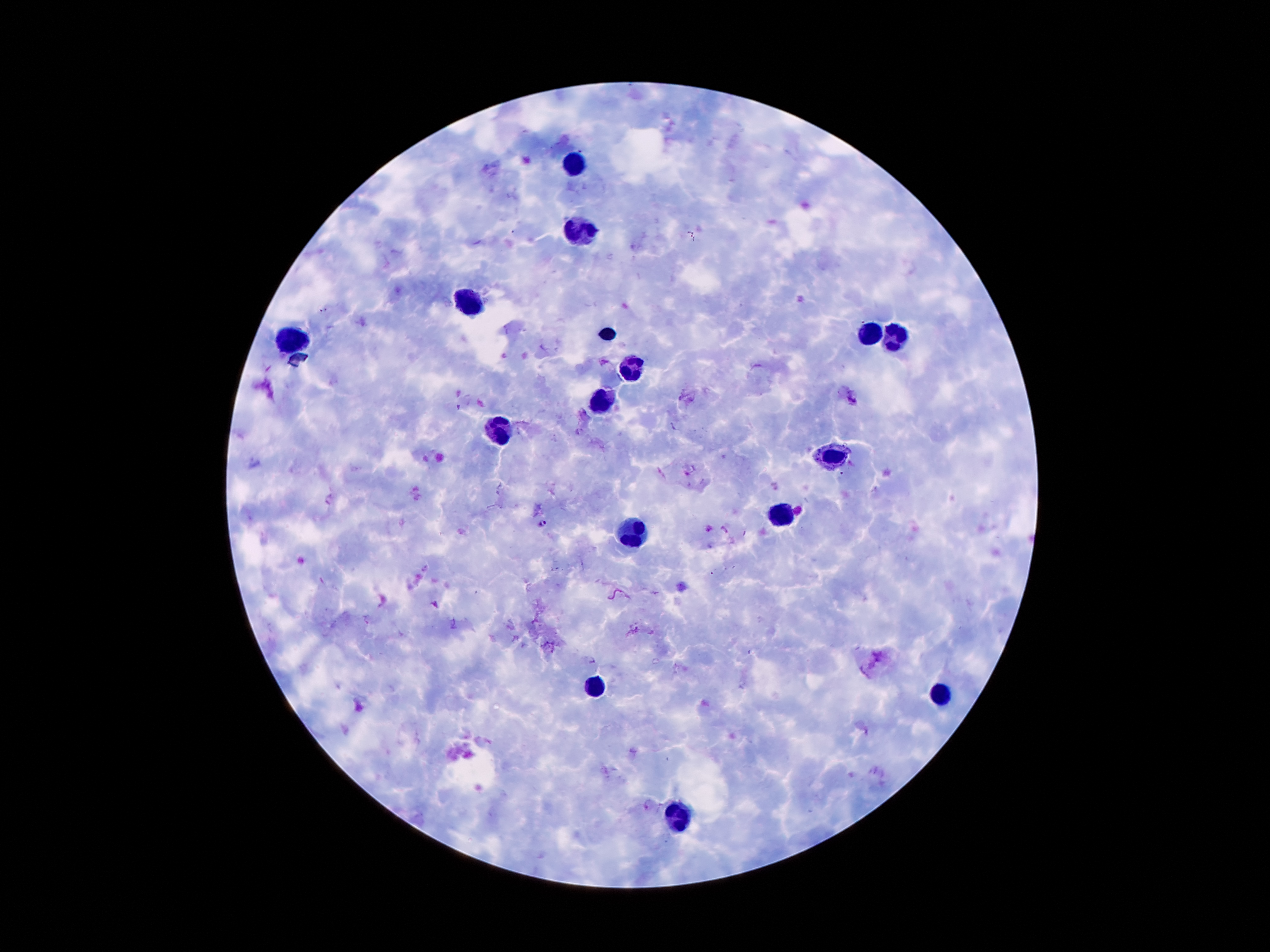

Approximate centers as (x, y) in pixels. Malaria parasite locations: (542, 523). Leukocyte locations: (574, 159), (579, 229), (467, 303), (604, 333), (867, 333), (895, 336), (293, 340), (634, 368), (602, 404), (497, 434), (826, 458), (783, 516), (635, 536), (597, 683), (941, 692), (679, 817). Single field of view. Thick peripheral-blood smear. 100x magnification. Giemsa-stained preparation. Patient malaria status: positive for Plasmodium falciparum. Image is 1270×952 pixels. Photographed through the microscope eyepiece with a smartphone camera.